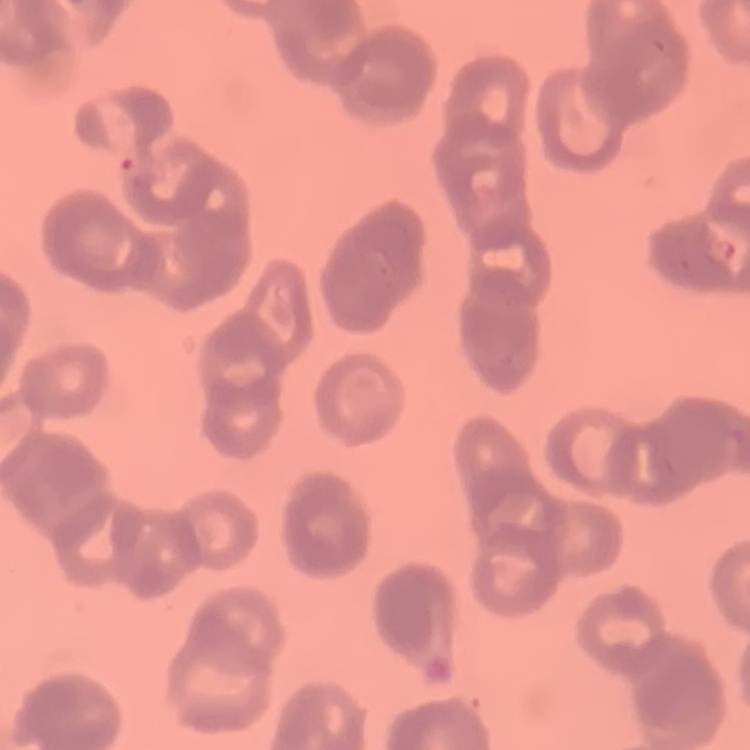
The red blood cells show rouleaux formation. Field's or Giemsa stain. Square crop of a larger photomicrograph. Thin blood smear.